Identify the parasite.
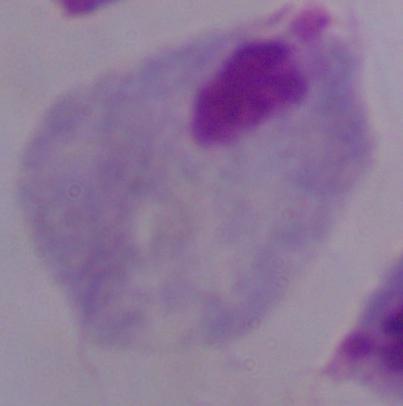

This is a trichomonad.

1000x magnification. Micrograph.